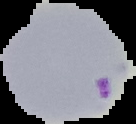

Summary:
  - Image size: 136×124 pixels
  - Preparation: thin blood film
  - Image type: cell region segmented out of the field of view; surrounding area masked to black
  - Malaria status: parasitized